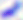

Summary:
  - Magnification: 400x
  - Identification: Toxoplasma gondii
  - Modality: micrograph